Describe the morphology of the erythrocytes.
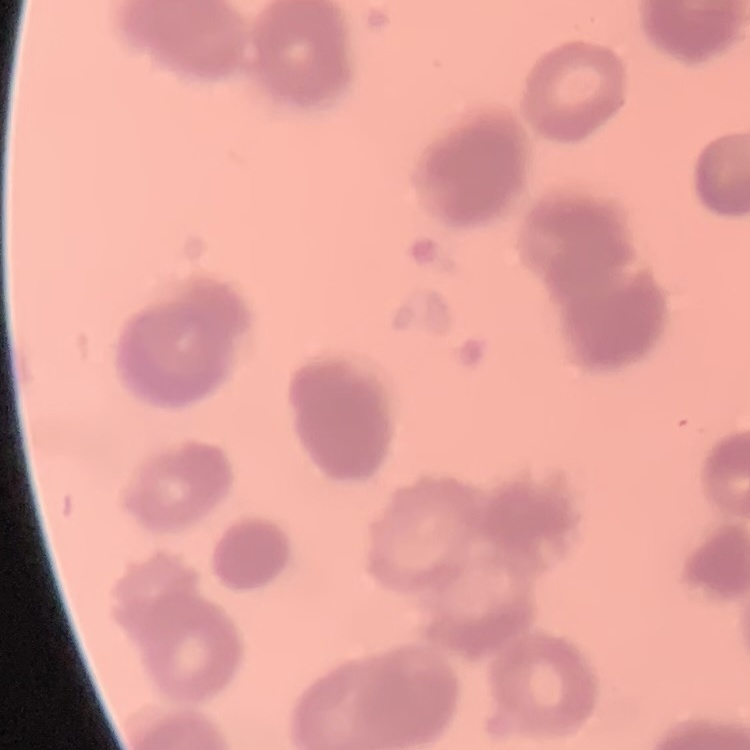

They show rouleaux formation.

Summary:
  - Stain: Field's or Giemsa
  - Image type: square crop of a larger photomicrograph
  - Preparation: thin blood smear